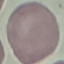 Result: no malaria parasites seen. Thin smear of blood. Giemsa stain. Photographed with a smartphone camera at the microscope eyepiece. Cell patch, automatically extracted from a larger field of view and resized to 64 × 64 pixels.